Assess the morphology of the erythrocytes.
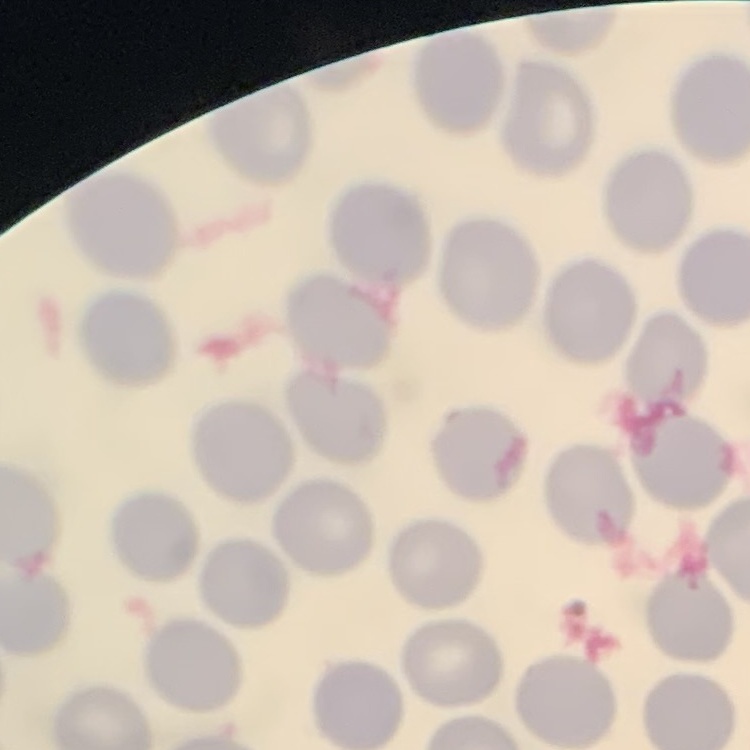
No rouleaux formation.

preparation = thin peripheral smear
image type = one tile cut from a larger photomicrograph
stain = Field's or Giemsa